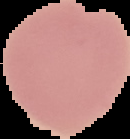
{
  "preparation": "thin blood film",
  "malaria_status": "uninfected",
  "image_size": "130×139 pixels",
  "image_type": "segmented cell region with the area outside set to black"
}